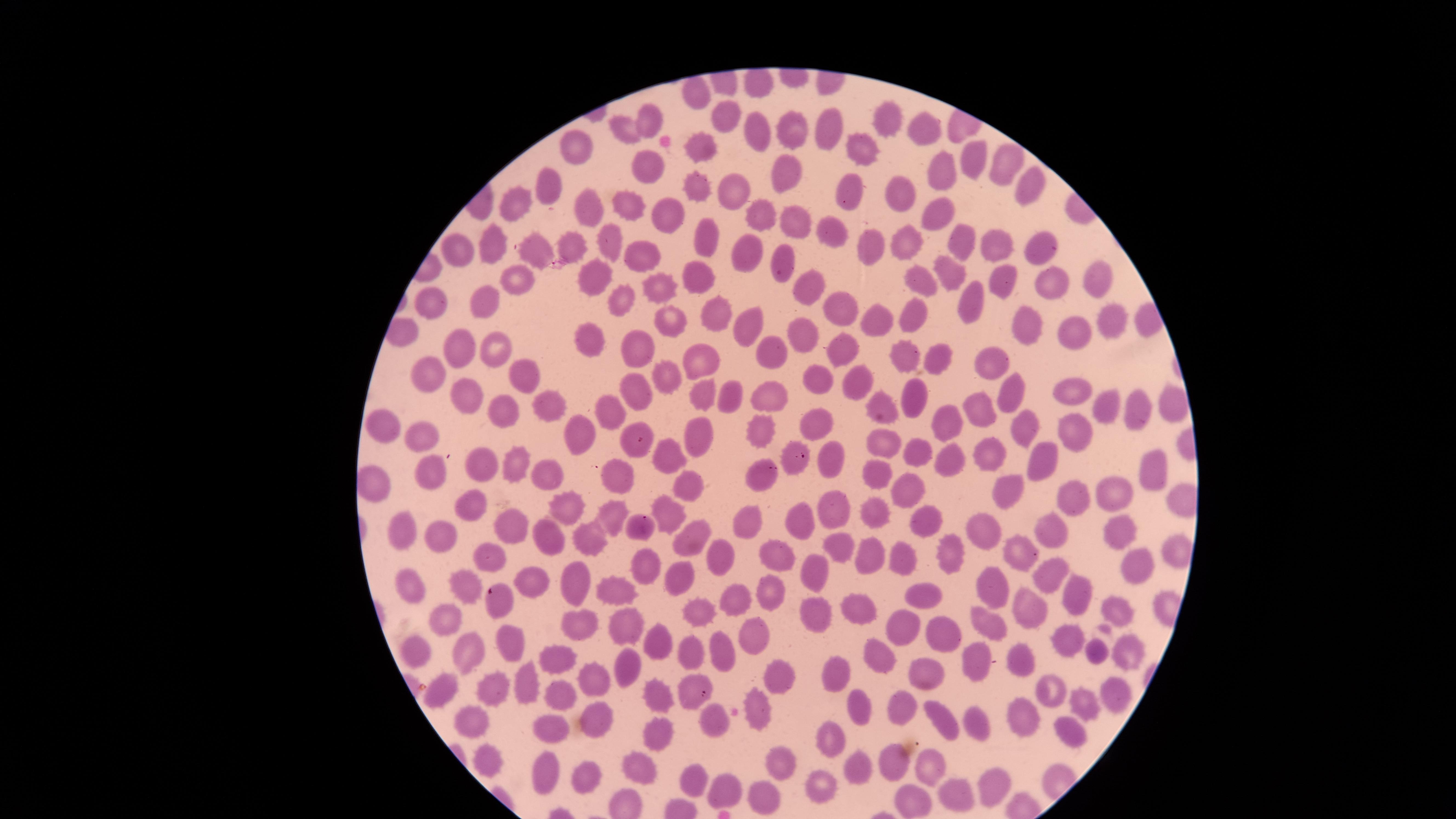
{
  "uninfected_red_blood_cells": "approximate marker points as [x, y] in pixels: [729, 114], [883, 116], [653, 123], [921, 123], [830, 125], [627, 126], [792, 129], [762, 132], [698, 145], [573, 151], [858, 154], [977, 159], [787, 164], [1002, 166], [644, 167], [941, 171], [1026, 179], [551, 185], [692, 186], [852, 190], [896, 192], [732, 195], [513, 206], [627, 207], [937, 211], [587, 214], [668, 215], [764, 218], [794, 222], [831, 232], [607, 239], [704, 240], [958, 242], [903, 244], [1004, 244], [1043, 245], [488, 246], [873, 246], [567, 248], [463, 249], [746, 253], [535, 257], [641, 257], [783, 262], [949, 272], [694, 273], [592, 274], [998, 274], [923, 276], [1103, 278], [521, 282], [658, 284], [1054, 284], [806, 288], [968, 294], [437, 302], [482, 302], [619, 302], [840, 307], [706, 309], [1114, 317], [873, 319], [671, 320], [909, 321], [752, 323], [1030, 325], [802, 331], [1081, 331], [594, 338], [838, 344], [494, 346], [463, 347], [645, 347], [773, 354], [904, 356], [939, 356], [698, 357], [991, 360], [434, 367], [521, 373], [816, 375], [663, 378], [854, 379], [639, 384], [1008, 390], [1081, 390], [707, 393], [771, 395], [732, 397], [471, 398], [914, 399], [878, 401], [616, 405], [547, 407], [987, 408], [1140, 408], [1108, 409], [500, 415], [948, 418], [1021, 421], [379, 423], [814, 425], [757, 428], [1069, 429], [629, 434], [698, 437], [418, 438], [587, 439], [878, 442], [912, 447], [1041, 451], [791, 452], [985, 452], [944, 454], [677, 458], [519, 460], [836, 460], [1158, 464], [488, 470], [878, 471], [426, 477], [685, 477], [763, 478], [559, 480], [622, 483], [373, 484], [1002, 486], [1115, 488], [909, 493], [1076, 493], [473, 504], [573, 507], [870, 508], [832, 509], [663, 513], [611, 514], [805, 514], [642, 521], [926, 522], [750, 523], [513, 524], [1050, 525], [1112, 527], [400, 531], [437, 533], [554, 533], [990, 533], [686, 536], [593, 537], [837, 543], [1018, 552], [486, 553], [870, 554], [777, 556], [725, 558], [949, 558], [903, 559], [1138, 564], [815, 569], [646, 570], [680, 576], [1044, 578], [540, 583], [409, 584], [471, 584], [582, 586], [614, 589], [997, 590], [1069, 590], [915, 596], [770, 597], [500, 598], [736, 598], [1111, 605], [858, 607], [816, 608], [704, 611], [1032, 613], [447, 616], [588, 624], [624, 626], [991, 626], [898, 629], [748, 633], [946, 634], [1069, 639], [665, 643], [513, 644], [1134, 646], [421, 649], [466, 650], [1095, 651], [718, 652], [696, 654], [878, 656], [1023, 659], [555, 661], [621, 661], [979, 662], [834, 673], [928, 674], [778, 678], [523, 679], [596, 681], [685, 683], [490, 684], [560, 689], [1054, 690], [439, 692], [1110, 696], [661, 701], [757, 703], [1072, 703], [861, 704], [901, 712], [937, 713], [1021, 715], [475, 717], [714, 718], [598, 720], [981, 724], [555, 727], [659, 734], [1074, 735], [831, 737], [484, 753], [887, 759], [782, 763], [931, 765], [638, 766], [854, 766], [584, 773], [545, 774], [687, 778], [822, 784], [987, 787], [726, 793], [763, 794], [955, 795], [914, 798]",
  "field_of_view": "single",
  "visible_region": "circular",
  "stain": "Giemsa",
  "image_size": "1456×819 pixels",
  "presence": "no malaria parasites identified",
  "preparation": "thin blood smear",
  "capture": "smartphone photograph through the microscope eyepiece"
}